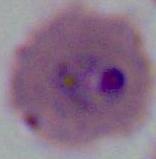

Summary:
  - Modality: micrograph
  - Identification: Plasmodium
  - Magnification: 400x or 1000x